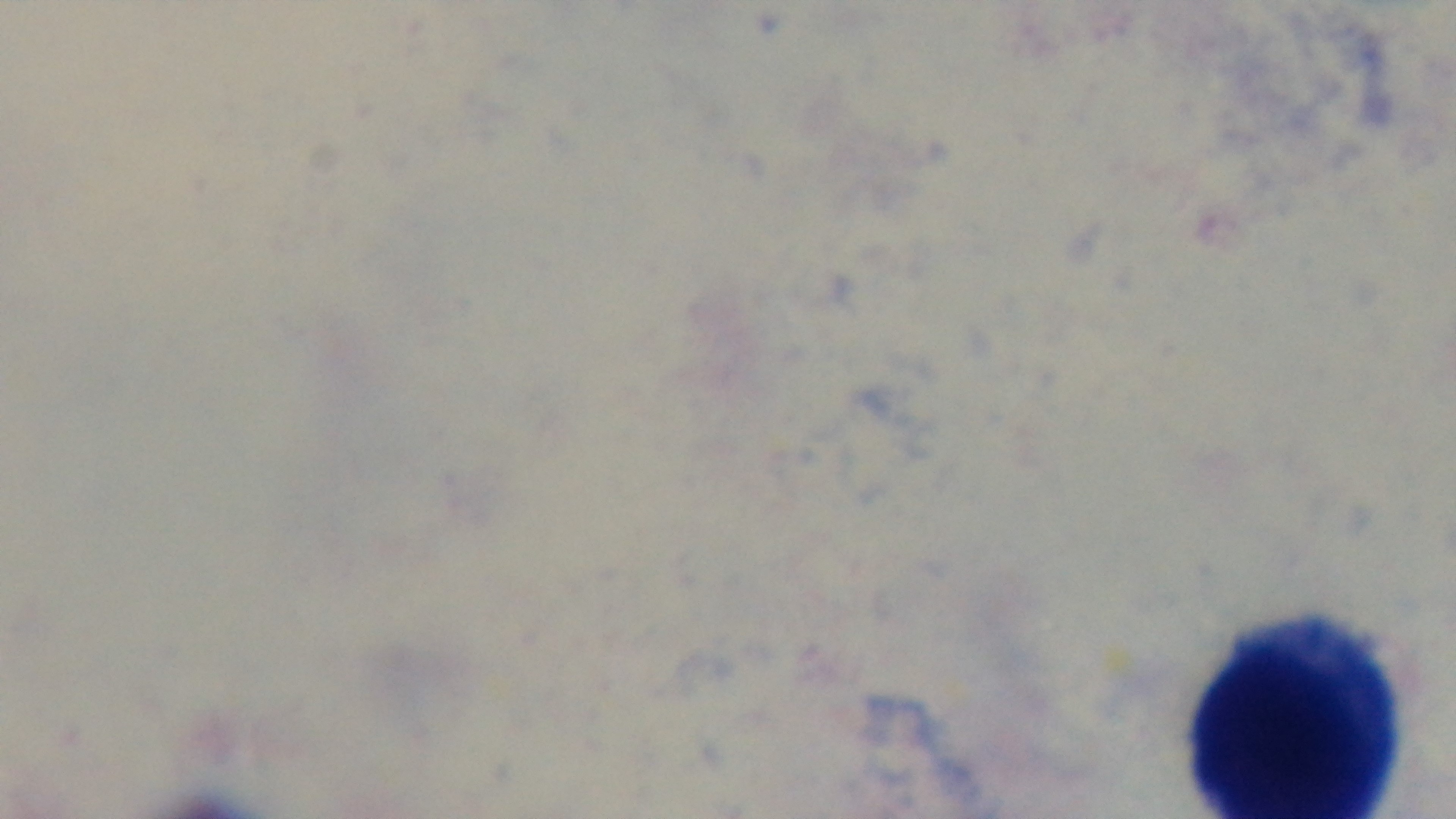

modality: light microscopy
objective: 100x oil immersion
malaria_status: negative
capture: mounted 4K digital camera
preparation: thick
stain: Giemsa
field_of_view: single